Evaluate for parasitized red blood cells.
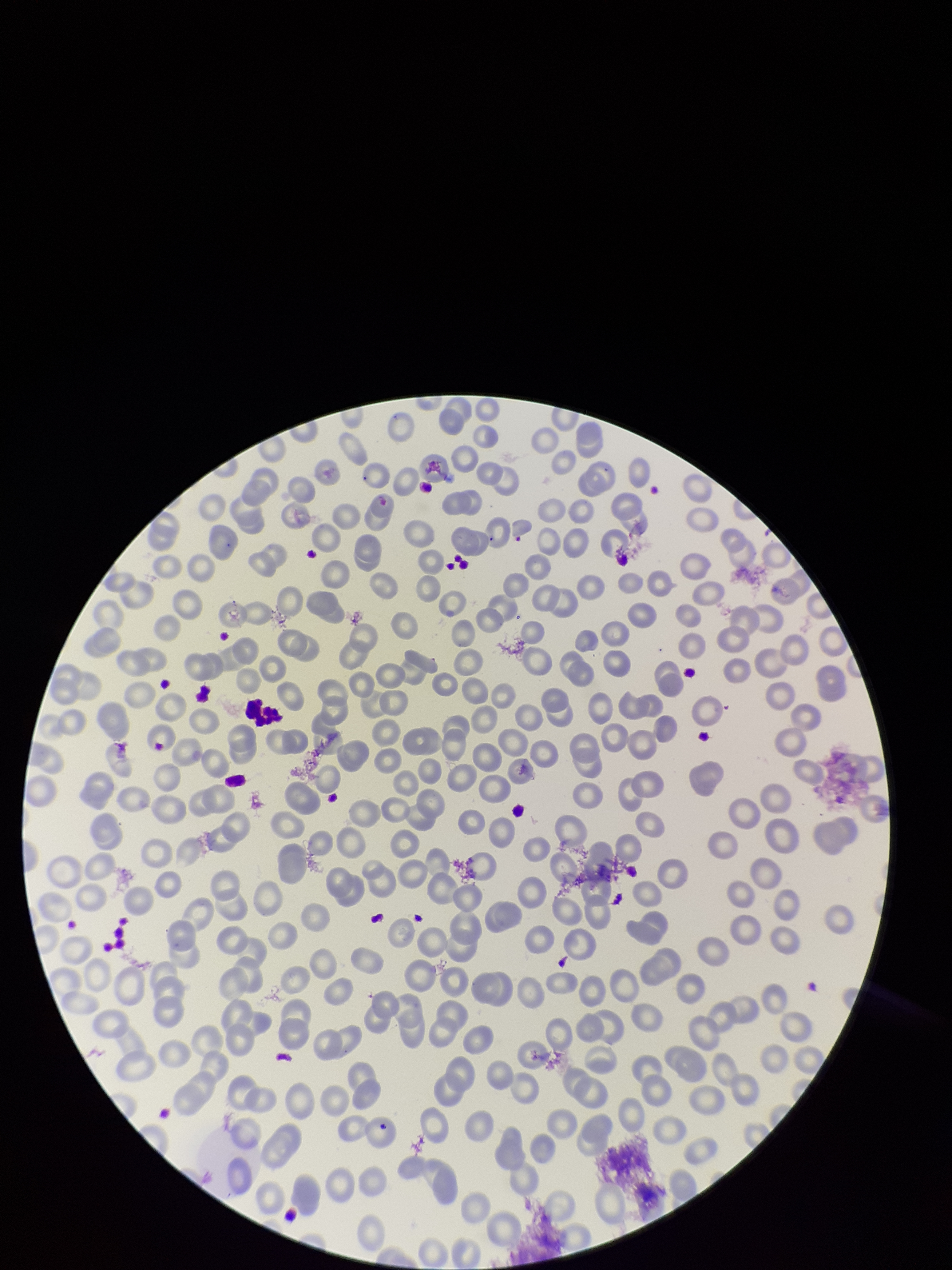
None identified.

Summary:
  - Preparation: thin
  - Field of view: one from this slide
  - Stain: Giemsa
  - Patient malaria status: infected
  - Species reported for this patient: Plasmodium falciparum
  - Red blood cell count: 250
  - Image size: 952×1270 pixels
  - Capture: smartphone photograph through the microscope eyepiece
  - Parasitized red blood cell count: 0